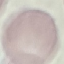

result = no malaria parasites seen
capture = smartphone through the microscope eyepiece
stain = Giemsa
image type = automatically extracted cell patch, resized to 64 × 64 pixels
preparation = thin blood film